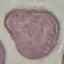

Malaria status: uninfected. Giemsa-stained preparation. Thin blood film. Cell patch, automatically extracted from a larger field of view and resized to 64 × 64 pixels. Acquired by smartphone through the microscope eyepiece.